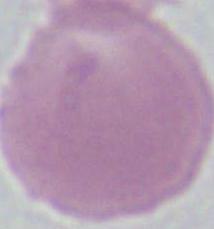
Summary:
  - Identification: red blood cell
  - Magnification: 1000x
  - Modality: micrograph